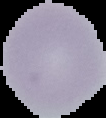
{
  "result": "no Plasmodium parasites detected",
  "image_size": "106×118 pixels",
  "image_type": "segmented cell region with the area outside set to black",
  "preparation": "thin blood film"
}